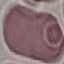

Malaria status: uninfected. Thin blood smear. Cell patch, automatically extracted from a larger field of view and resized to 64 × 64 pixels. Acquired by smartphone through the microscope eyepiece. Giemsa-stained preparation.